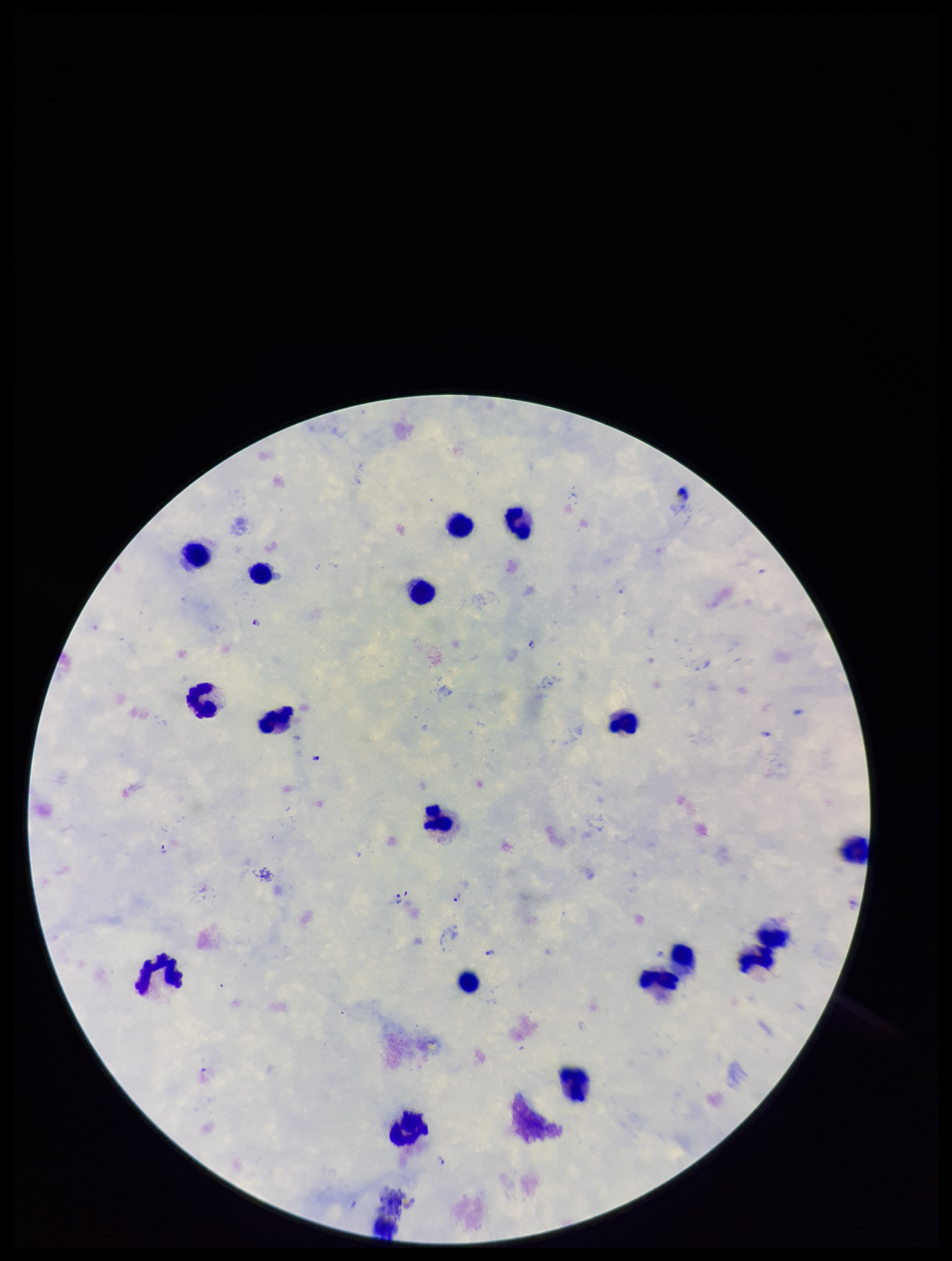

Summary:
  - Leukocyte count: 19
  - Species reported for this patient: Plasmodium falciparum
  - Preparation: thick blood smear
  - Stain: Giemsa
  - Parasite count: 9
  - Image size: 952×1261 pixels
  - Plasmodium parasites: seen
  - Field of view: one from this slide
  - Capture: smartphone photograph through the microscope eyepiece
  - Patient malaria status: positive